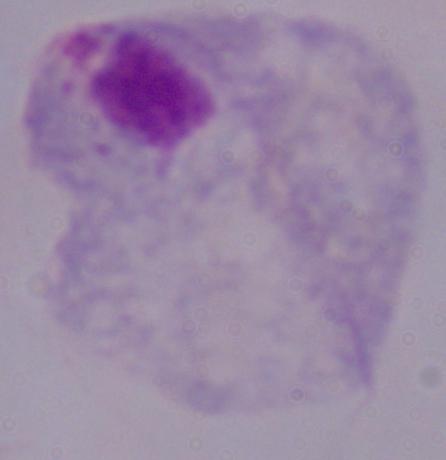
identification = trichomonad
modality = micrograph
magnification = 1000x